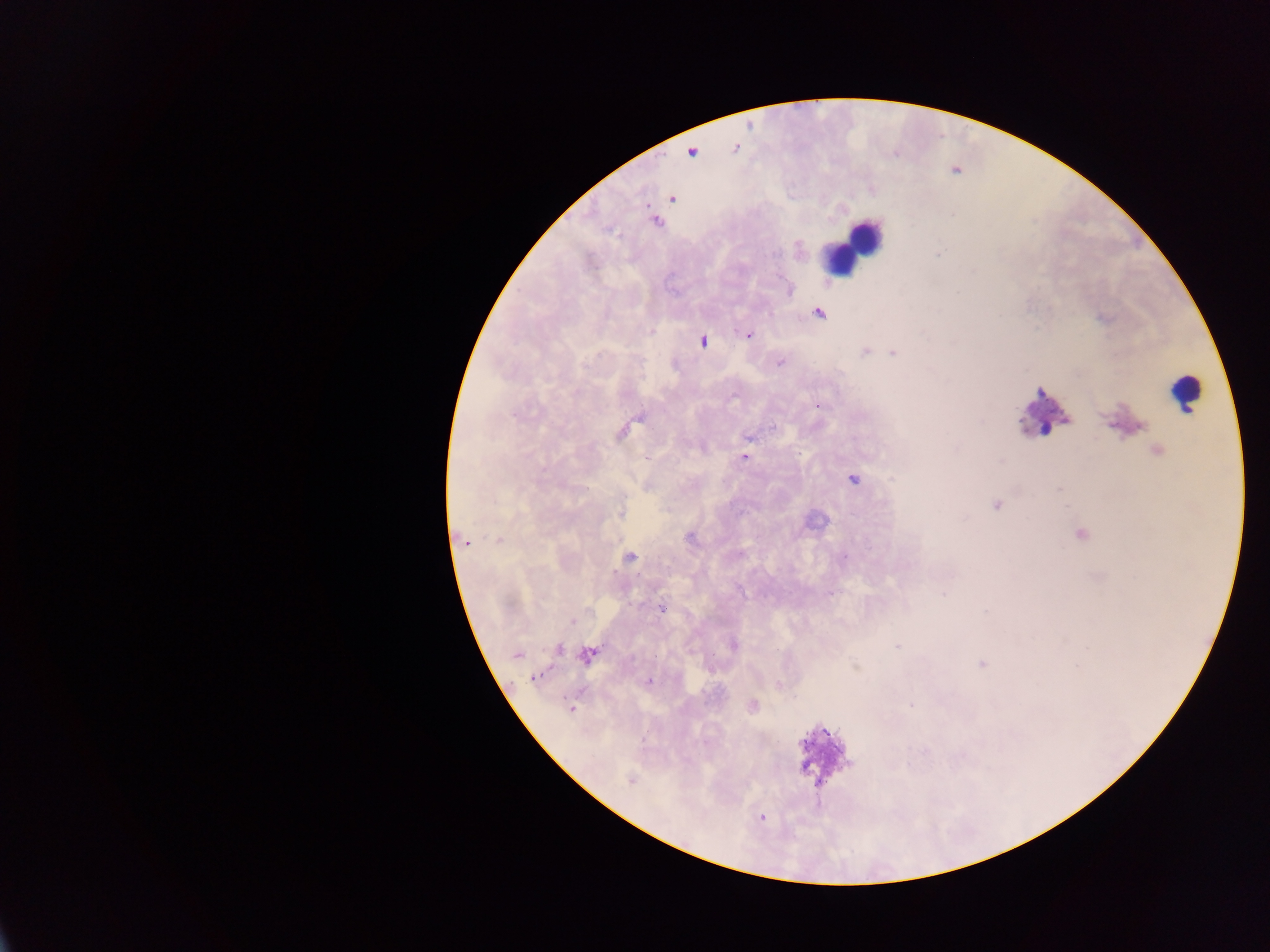

Approximate centers as (x, y) in pixels.
Summary:
  - Malaria parasite locations: (671, 199), (953, 214), (655, 222), (938, 254), (819, 312), (748, 334), (702, 341), (865, 351), (894, 353), (780, 362), (819, 405), (772, 428), (622, 433), (748, 437), (1158, 451), (744, 457), (853, 479), (996, 505), (620, 513), (1082, 534), (498, 539), (690, 539), (465, 542), (844, 557), (631, 558), (831, 593), (943, 594), (661, 609), (572, 620), (734, 645), (896, 647), (559, 649), (517, 654), (588, 655), (981, 664), (535, 677), (648, 682), (778, 684), (752, 705), (910, 705), (570, 709), (631, 780), (761, 818)
  - Leukocyte locations: (854, 244), (1184, 392), (1046, 415), (824, 752)
  - Image size: 1270×952 pixels
  - Field of view: single
  - Capture: mobile-phone photograph through a microscope
  - Preparation: thick blood film
  - Country: Ghana